Name the parasite shown.
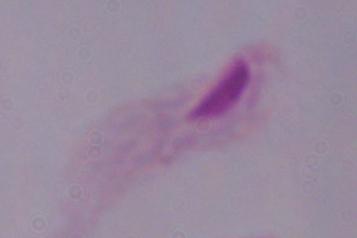

A trichomonad.

Summary:
  - Magnification: 1000x
  - Modality: micrograph